Name the parasite shown.
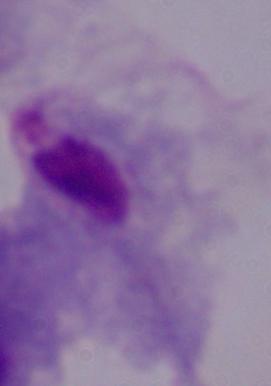
This is a trichomonad.

1000x magnification. Micrograph.